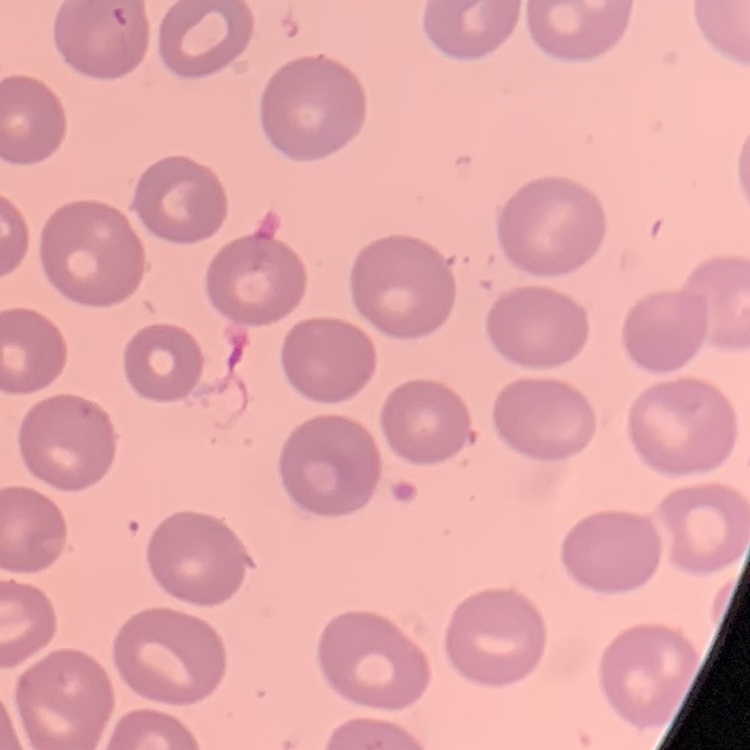
erythrocyte morphology = no rouleaux formation
preparation = thin blood smear
image type = square crop of a larger photomicrograph
stain = Field's or Giemsa